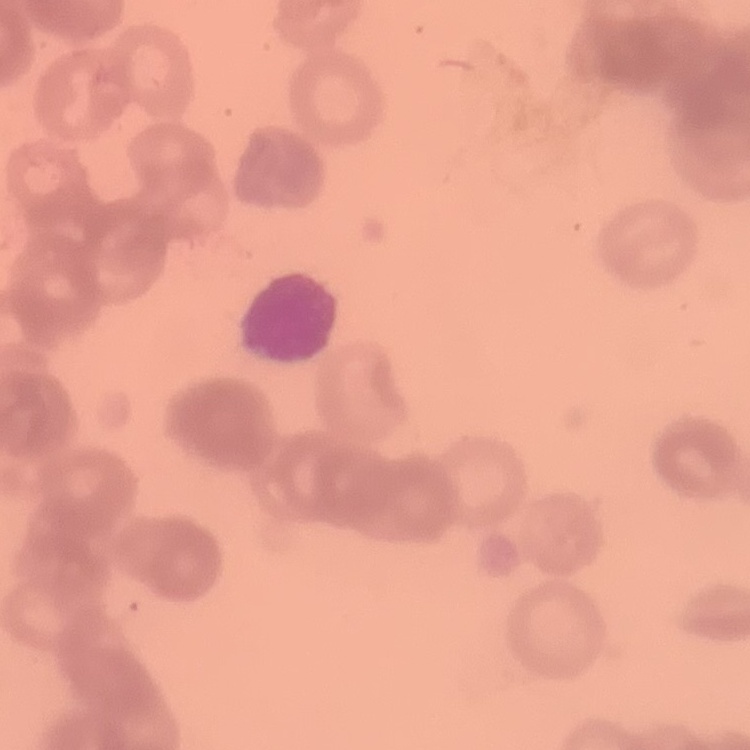
Summary:
  - Erythrocyte morphology: rouleaux formation
  - Image type: square crop of a larger photomicrograph
  - Preparation: thin peripheral smear
  - Stain: Field's or Giemsa